Classify this cell by malaria status.
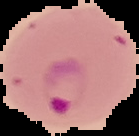

Parasitized.

Image is 139×136 pixels. Cell region segmented out of the field of view; the surrounding area is masked to black. From a thin blood smear.